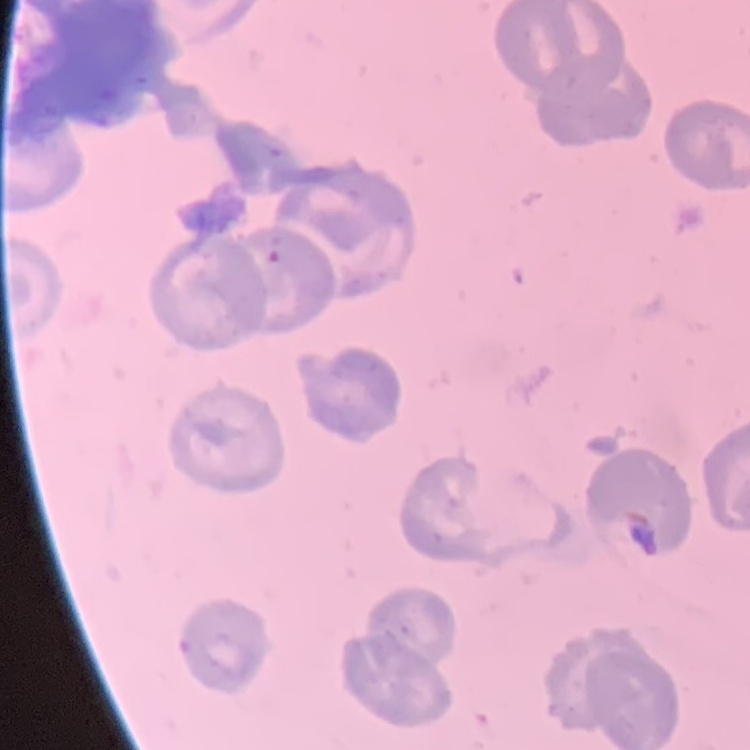

Summary:
  - Red blood cell morphology: no rouleaux formation
  - Image type: square crop of a larger photomicrograph
  - Preparation: thin peripheral smear
  - Stain: Field's or Giemsa